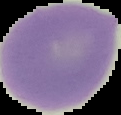
image type = cell region segmented out of the field of view; surrounding area masked to black
result = no malaria parasites detected
image size = 121×115 pixels
preparation = thin blood smear